Assess the morphology of the red blood cells.
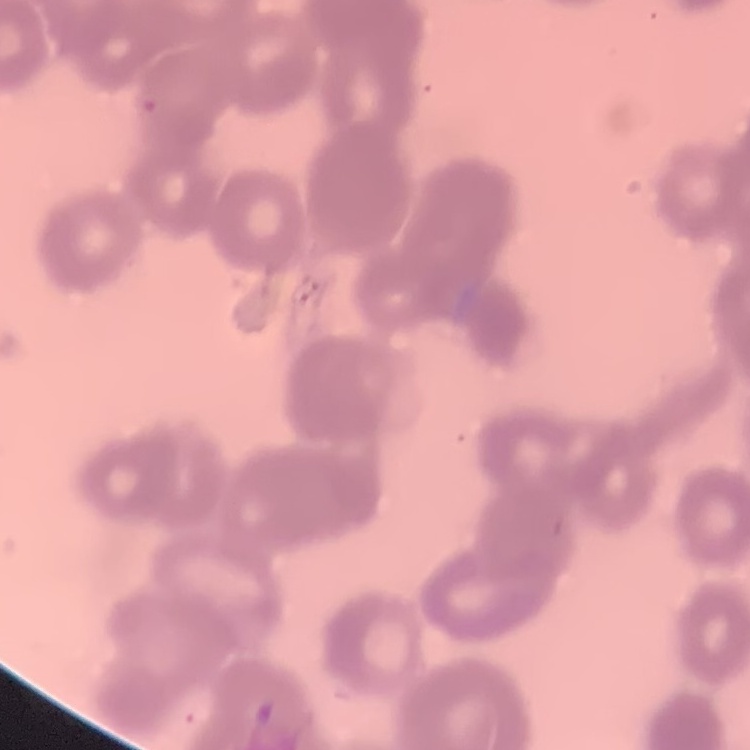
They show rouleaux formation.

Square crop of a larger photomicrograph. Stained with either Field's or Giemsa. Thin blood smear.